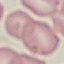
malaria status = uninfected
preparation = thin blood smear
stain = Giemsa
capture = smartphone through the microscope eyepiece
image type = automatically extracted cell patch, resized to 64 × 64 pixels